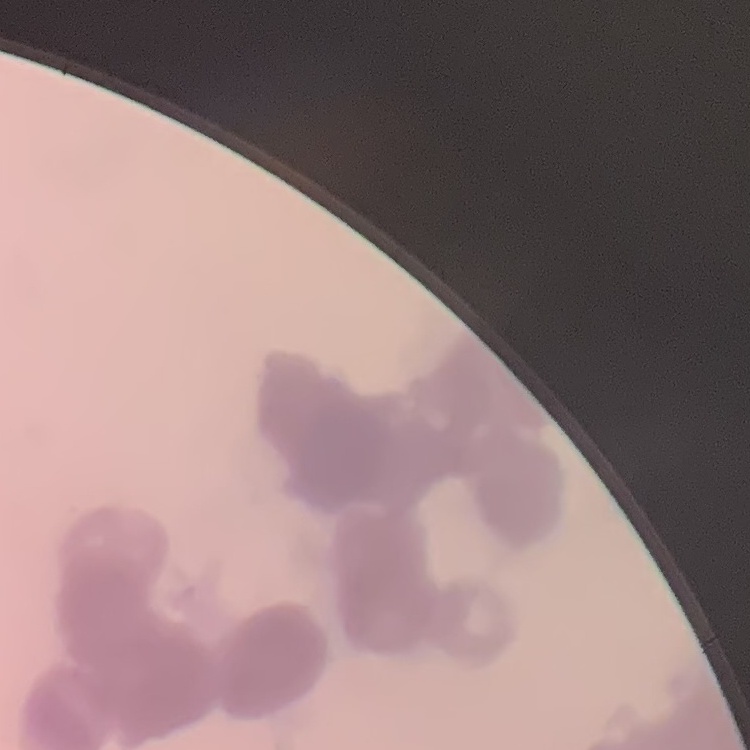
Summary:
  - Red blood cell morphology: rouleaux formation
  - Stain: Field's or Giemsa
  - Image type: one tile cut from a larger photomicrograph
  - Preparation: thin blood smear